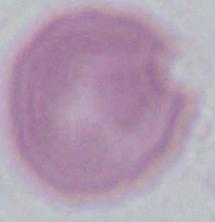

identification = red blood cell
modality = micrograph
magnification = 1000x